Outline each Plasmodium malariae-infected red blood cell.
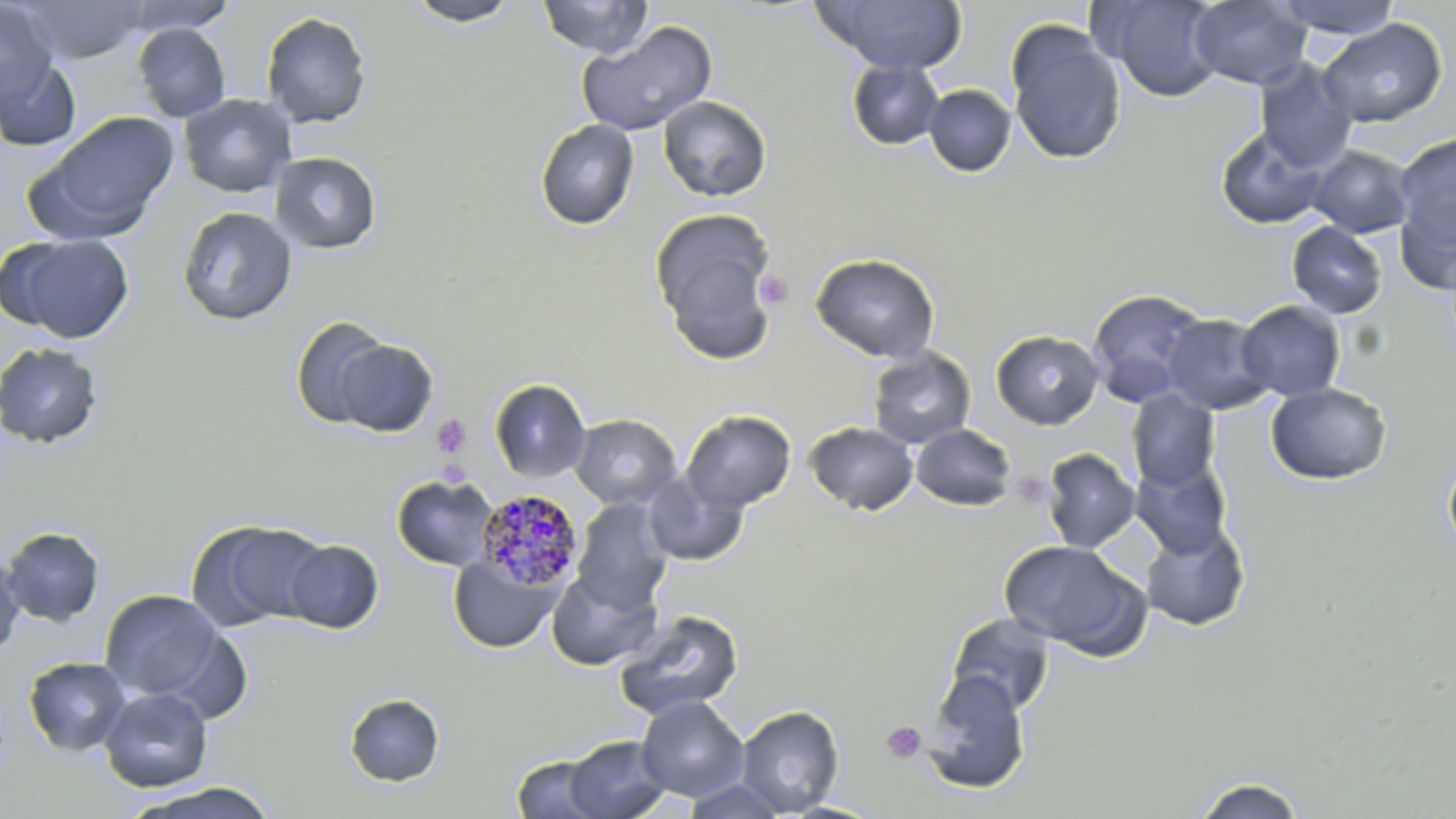
Approximate bounding boxes as (x1,y1)-(x2,y2) corner pairs in pixels.
Plasmodium malariae-infected red blood cells: (476,489)-(584,590).

Summary:
  - Platelet locations: (756,270)-(792,310), (432,414)-(473,459), (880,721)-(927,764)
  - Uninfected red blood cell locations: (17,0)-(148,63), (120,0)-(237,34), (405,0)-(524,27), (537,0)-(653,58), (813,0)-(969,75), (1095,0)-(1227,102), (1188,0)-(1312,89), (1272,0)-(1403,38), (0,3)-(59,107), (260,11)-(372,129), (1317,18)-(1448,128), (1005,19)-(1127,166), (577,21)-(718,137), (132,22)-(231,122), (0,56)-(82,152), (1254,59)-(1358,172), (847,60)-(944,150), (923,84)-(1016,177), (178,93)-(297,198), (657,95)-(772,202), (35,112)-(179,238), (535,118)-(639,230), (1215,125)-(1330,230), (1394,132)-(1456,250), (1306,144)-(1415,238), (270,151)-(381,255), (1397,194)-(1455,294), (177,206)-(298,326), (650,209)-(780,361), (1286,221)-(1387,319), (4,233)-(135,343), (809,252)-(940,363), (1086,289)-(1212,407), (1235,300)-(1346,402), (1161,313)-(1275,415), (290,316)-(393,429), (990,329)-(1105,429), (332,338)-(439,438), (0,342)-(103,449), (868,347)-(977,449), (488,378)-(591,483), (1264,382)-(1391,485), (1126,390)-(1220,493), (681,410)-(797,513), (570,414)-(682,510), (804,421)-(918,517), (910,424)-(1017,511), (1040,448)-(1140,553), (1442,448)-(1456,563), (1130,457)-(1233,558), (641,470)-(748,567), (391,474)-(500,572), (571,498)-(673,612), (187,518)-(330,631), (1138,520)-(1251,633), (1,526)-(105,627), (283,539)-(384,634), (998,540)-(1148,659), (0,551)-(25,661), (448,554)-(561,654), (546,568)-(662,670), (99,589)-(224,702), (614,608)-(745,721), (944,613)-(1057,717), (23,656)-(131,756), (920,671)-(1031,794), (99,687)-(213,792), (344,693)-(445,787), (635,696)-(749,801), (735,705)-(844,816), (563,735)-(673,819), (511,754)-(609,818), (1190,774)-(1308,818), (680,777)-(789,818), (121,781)-(282,818)
  - Slide-level diagnosis: Plasmodium malariae
  - Preparation: thin blood film
  - Stain: May-Grünwald-Giemsa
  - Modality: light microscopy
  - Magnification: 1000x
  - Field of view: single
  - Image size: 1456×819 pixels